Name the parasite shown.
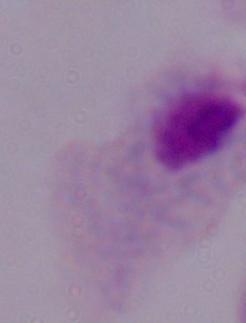
This is a trichomonad.

modality: micrograph
magnification: 1000x